Identify the blood parasite species.
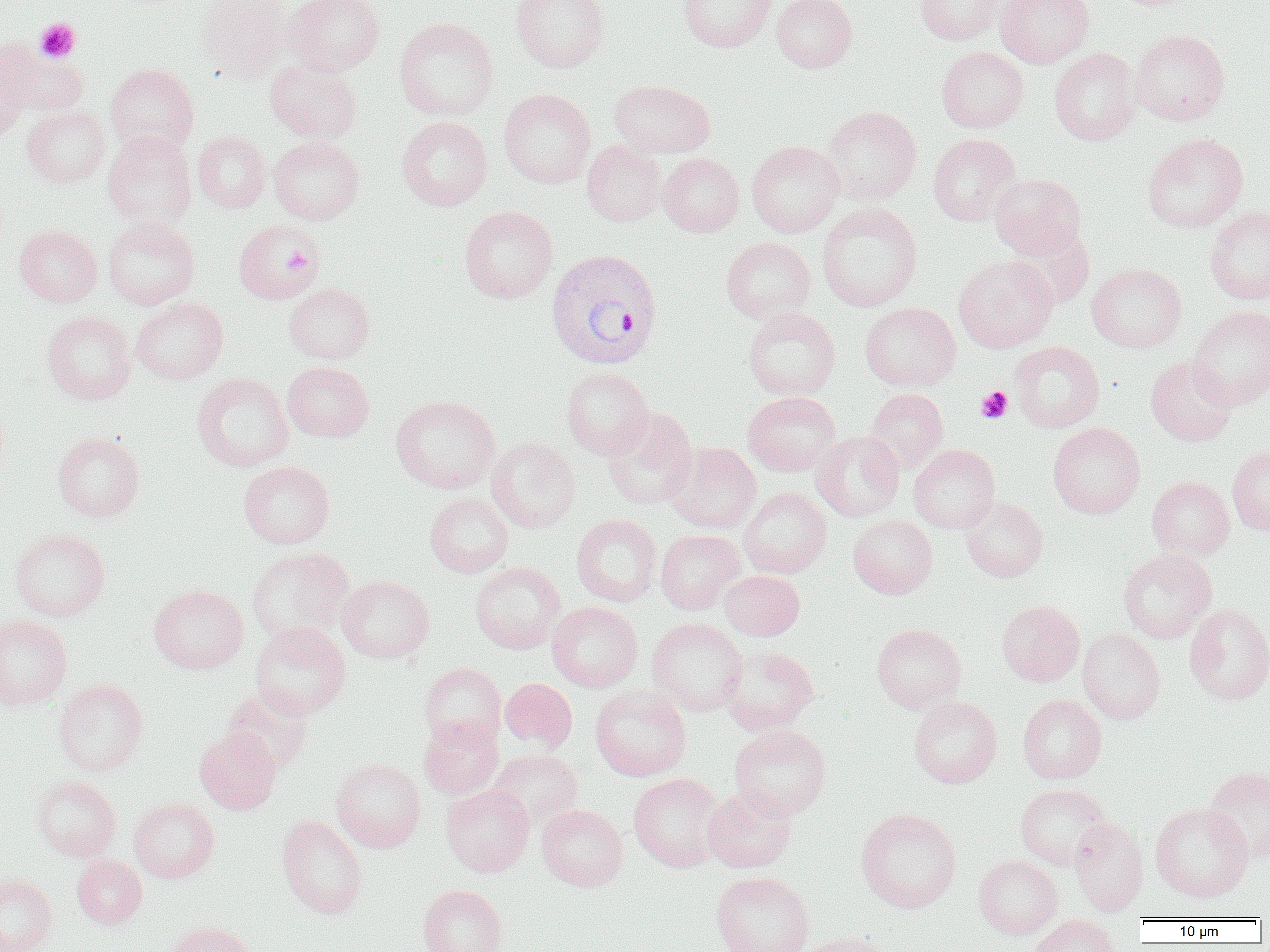

Plasmodium vivax.

{
  "magnification": "1000x",
  "image_size": "1270×952 pixels",
  "preparation": "thin blood film",
  "uninfected_red_blood_cell_locations": "approximate bounding boxes as (x1,y1)-(x2,y2) corner pairs in pixels: (197,0)-(290,80), (286,0)-(385,76), (510,0)-(609,73), (678,0)-(775,52), (772,0)-(858,73), (915,0)-(1004,45), (995,0)-(1094,67), (394,17)-(499,120), (1130,29)-(1230,125), (1,40)-(88,117), (0,43)-(29,138), (936,46)-(1029,132), (1050,47)-(1140,145), (265,62)-(362,143), (105,63)-(200,157), (610,80)-(715,158), (498,88)-(596,188), (821,105)-(921,206), (22,106)-(110,188), (396,116)-(492,211), (193,131)-(271,212), (102,132)-(197,230), (1142,133)-(1248,232), (927,134)-(1021,225), (268,136)-(364,224), (582,139)-(667,226), (746,140)-(844,237), (658,153)-(744,236), (989,173)-(1087,259), (816,202)-(922,312), (459,204)-(558,303), (1205,206)-(1270,305), (103,217)-(200,309), (234,219)-(322,303), (1006,224)-(1095,308), (15,225)-(102,307), (721,237)-(815,324), (953,254)-(1058,352), (1087,263)-(1187,353), (284,283)-(375,364), (131,298)-(228,384), (860,302)-(960,391), (1188,306)-(1270,407), (743,307)-(840,399), (42,311)-(136,404), (1009,341)-(1104,432), (1145,355)-(1237,445), (282,361)-(374,442), (562,367)-(653,460), (192,372)-(294,472), (866,388)-(948,471), (742,391)-(841,476), (391,395)-(500,493), (601,406)-(698,510), (1048,422)-(1145,518), (810,429)-(905,522), (52,431)-(144,522), (486,436)-(581,533), (664,442)-(761,533), (909,444)-(1000,533), (1228,445)-(1270,535), (238,461)-(335,549), (1147,476)-(1234,560), (738,487)-(832,578), (424,492)-(513,577), (960,497)-(1048,582), (572,514)-(662,607), (848,515)-(937,598), (10,528)-(110,622), (655,530)-(745,614), (246,547)-(354,644), (1118,549)-(1217,642), (469,561)-(565,653), (719,570)-(804,640), (337,575)-(434,663), (149,584)-(249,674), (996,600)-(1084,686), (547,601)-(643,692), (1184,604)-(1270,704), (0,614)-(73,710), (647,617)-(747,716), (250,621)-(351,719), (871,623)-(967,713), (1077,628)-(1165,724), (720,647)-(819,735), (419,663)-(506,748), (500,678)-(577,753), (54,679)-(148,775), (590,685)-(691,781), (223,688)-(314,774), (1017,693)-(1107,784), (909,696)-(1002,788), (419,716)-(503,799), (729,724)-(831,820), (194,726)-(281,814), (487,749)-(582,830), (332,757)-(426,852), (1203,766)-(1270,863), (628,773)-(726,872), (32,775)-(121,860), (1015,784)-(1112,870), (441,785)-(534,876), (702,786)-(797,873), (129,798)-(219,882), (1150,802)-(1253,902), (536,804)-(628,891), (855,807)-(961,912), (277,814)-(367,919), (1068,817)-(1148,916), (72,854)-(147,928), (974,855)-(1062,939), (711,871)-(814,952), (0,874)-(57,952), (417,884)-(507,952), (1029,914)-(1122,952), (163,921)-(256,952), (795,932)-(894,952)",
  "field_of_view": "one of a larger specimen",
  "plasmodium_vivax_infected_red_blood_cell_locations": "approximate bounding boxes as (x1,y1)-(x2,y2) corner pairs in pixels: (546,248)-(663,370)",
  "modality": "optical microscopy",
  "platelet_locations": "approximate bounding boxes as (x1,y1)-(x2,y2) corner pairs in pixels: (35,18)-(81,62), (283,246)-(314,276), (976,386)-(1013,423)"
}